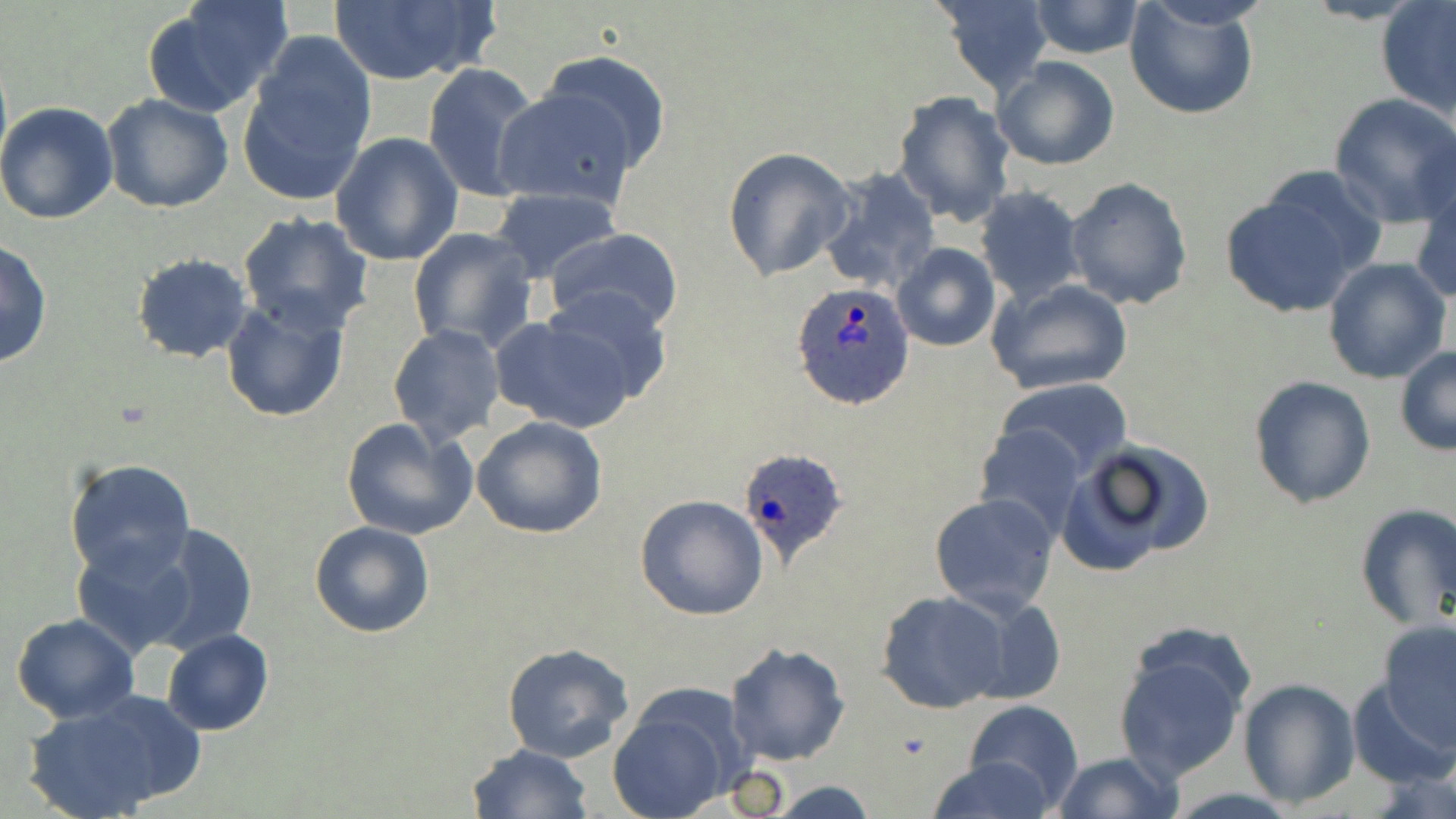
slide-level diagnosis = Plasmodium ovale
magnification = 1000x
Plasmodium ovale-infected red blood cell locations = approximate bounding boxes as named x1/y1/x2/y2 corners in pixels: (x1=793, y1=282, x2=915, y2=410), (x1=736, y1=444, x2=847, y2=570)
image size = 1456×819 pixels
stain = May-Grünwald-Giemsa
uninfected red blood cell locations = approximate bounding boxes as named x1/y1/x2/y2 corners in pixels: (x1=327, y1=0, x2=498, y2=85), (x1=938, y1=0, x2=1055, y2=93), (x1=146, y1=1, x2=292, y2=114), (x1=1028, y1=1, x2=1143, y2=58), (x1=1124, y1=1, x2=1260, y2=120), (x1=1376, y1=3, x2=1456, y2=119), (x1=241, y1=35, x2=375, y2=201), (x1=540, y1=50, x2=672, y2=171), (x1=992, y1=56, x2=1119, y2=171), (x1=422, y1=62, x2=544, y2=203), (x1=495, y1=88, x2=637, y2=209), (x1=892, y1=91, x2=1016, y2=228), (x1=100, y1=92, x2=233, y2=214), (x1=1328, y1=93, x2=1456, y2=228), (x1=0, y1=100, x2=121, y2=224), (x1=330, y1=132, x2=463, y2=266), (x1=722, y1=146, x2=856, y2=281), (x1=817, y1=167, x2=942, y2=295), (x1=1411, y1=175, x2=1456, y2=306), (x1=1064, y1=176, x2=1193, y2=311), (x1=1219, y1=183, x2=1371, y2=317), (x1=974, y1=186, x2=1086, y2=306), (x1=490, y1=188, x2=622, y2=284), (x1=238, y1=213, x2=373, y2=336), (x1=408, y1=226, x2=539, y2=353), (x1=545, y1=227, x2=684, y2=334), (x1=0, y1=241, x2=52, y2=370), (x1=892, y1=242, x2=1000, y2=352), (x1=131, y1=253, x2=253, y2=364), (x1=1323, y1=258, x2=1451, y2=386), (x1=986, y1=277, x2=1134, y2=395), (x1=539, y1=285, x2=675, y2=405), (x1=219, y1=295, x2=350, y2=423), (x1=490, y1=314, x2=634, y2=433), (x1=387, y1=324, x2=505, y2=445), (x1=1396, y1=346, x2=1456, y2=455), (x1=1247, y1=375, x2=1376, y2=509), (x1=995, y1=378, x2=1135, y2=480), (x1=340, y1=416, x2=478, y2=540), (x1=472, y1=416, x2=607, y2=540), (x1=973, y1=424, x2=1087, y2=538), (x1=1062, y1=439, x2=1212, y2=573), (x1=64, y1=457, x2=195, y2=580), (x1=928, y1=490, x2=1060, y2=615), (x1=635, y1=494, x2=768, y2=620), (x1=1355, y1=505, x2=1455, y2=631), (x1=310, y1=522, x2=435, y2=637), (x1=143, y1=523, x2=259, y2=655), (x1=71, y1=539, x2=200, y2=659), (x1=877, y1=591, x2=1012, y2=714), (x1=11, y1=613, x2=140, y2=724), (x1=1378, y1=621, x2=1456, y2=752), (x1=1112, y1=627, x2=1253, y2=786), (x1=161, y1=629, x2=273, y2=736), (x1=725, y1=642, x2=850, y2=766), (x1=502, y1=643, x2=634, y2=761), (x1=1348, y1=677, x2=1453, y2=788), (x1=1237, y1=678, x2=1359, y2=807), (x1=609, y1=691, x2=741, y2=818), (x1=21, y1=699, x2=191, y2=819), (x1=964, y1=701, x2=1082, y2=813), (x1=467, y1=744, x2=593, y2=819), (x1=1050, y1=752, x2=1181, y2=819), (x1=924, y1=757, x2=1060, y2=818), (x1=770, y1=780, x2=878, y2=817)
modality = light microscopy
preparation = thin blood smear
field of view = single